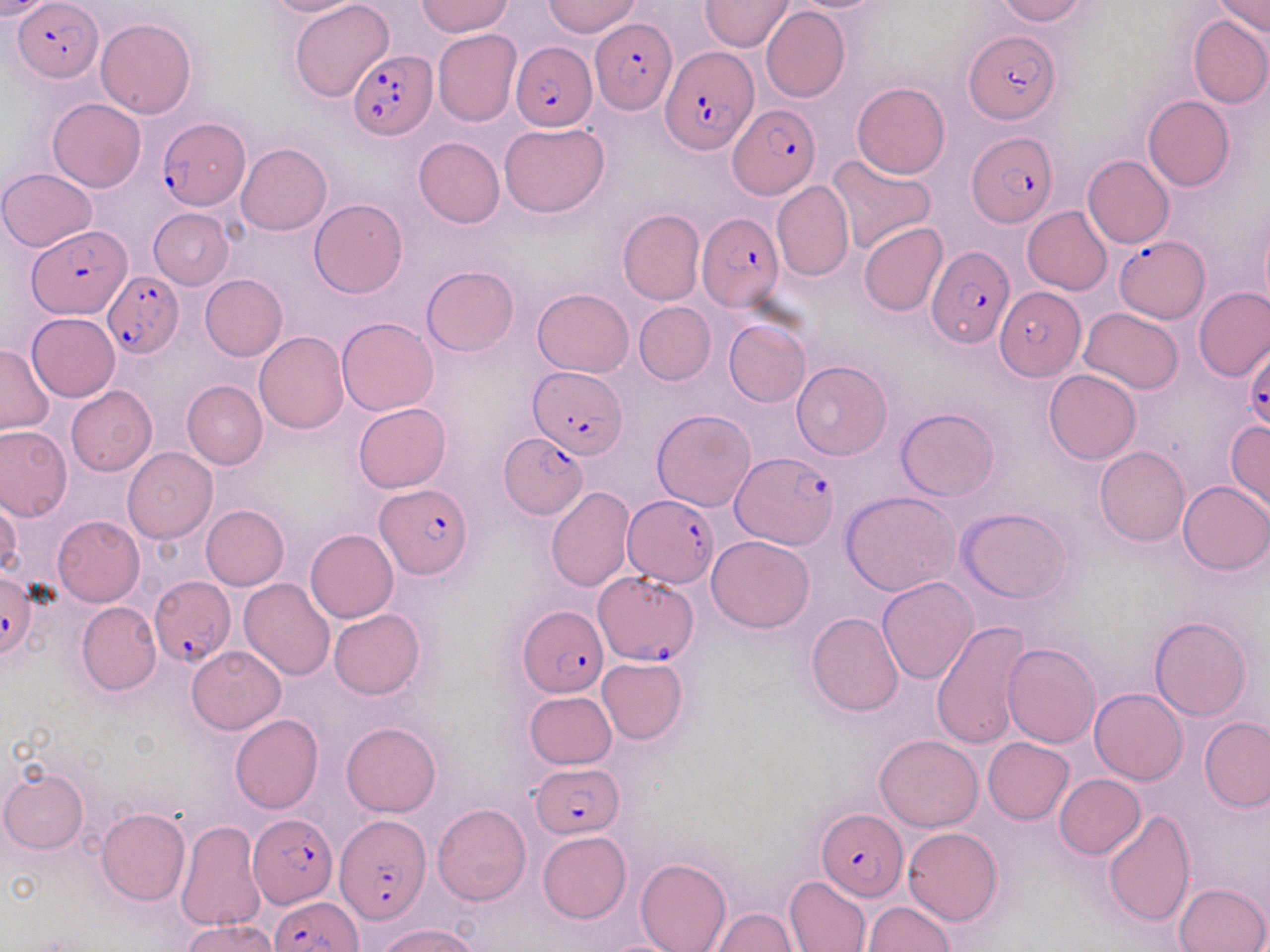
slide_level_diagnosis: Plasmodium falciparum
image_size: 1270×952 pixels
magnification: 1000x
modality: light microscopy
field_of_view: single
stain: May-Grünwald-Giemsa
uninfected_red_blood_cell_locations: 'approximate bounding boxes as (x1,y1)-(x2,y2) corner pairs in pixels: (0,0)-(56,19), (261,0)-(363,18), (543,0)-(640,37), (783,0)-(889,12), (995,0)-(1087,24), (1211,0)-(1269,38), (291,1)-(395,103), (417,1)-(513,37), (699,1)-(795,51), (761,5)-(850,102), (1188,14)-(1270,107), (96,18)-(197,118), (432,30)-(521,126), (851,82)-(949,179), (1143,95)-(1235,191), (47,98)-(146,192), (500,122)-(610,217), (413,136)-(505,228), (236,142)-(331,234), (826,153)-(936,253), (1084,155)-(1174,248), (0,169)-(98,251), (772,180)-(853,281), (309,199)-(407,298), (1023,205)-(1113,295), (149,208)-(234,289), (617,209)-(705,306), (1260,218)-(1270,317), (859,222)-(948,316), (422,266)-(519,357), (200,273)-(287,360), (1194,287)-(1270,382), (532,288)-(634,376), (634,302)-(715,385), (1080,308)-(1183,393), (27,313)-(121,400), (338,317)-(438,416), (723,319)-(809,407), (254,331)-(349,434), (0,344)-(53,434), (791,360)-(891,459), (1043,369)-(1140,464), (182,380)-(267,469), (66,386)-(156,475), (353,403)-(449,493), (896,407)-(998,501), (652,409)-(757,511), (1227,420)-(1270,513), (0,425)-(72,521), (1095,446)-(1189,545), (122,448)-(217,543), (1178,481)-(1270,574), (546,486)-(635,591), (842,491)-(959,596), (0,494)-(22,579), (200,504)-(289,590), (956,508)-(1070,602), (53,516)-(145,606), (306,528)-(398,623), (706,535)-(814,632), (878,576)-(979,684), (239,578)-(336,681), (76,601)-(161,696), (328,610)-(424,699), (806,612)-(903,716), (1149,616)-(1252,721), (931,619)-(1032,749), (1003,642)-(1100,746), (186,645)-(285,733), (597,656)-(688,744), (1090,687)-(1187,785), (524,691)-(616,768), (230,714)-(323,815), (1201,717)-(1270,814), (342,721)-(441,816), (875,734)-(984,831), (984,737)-(1073,824), (1,766)-(89,853), (1053,774)-(1145,859), (432,802)-(532,905), (96,808)-(190,904), (1102,808)-(1196,928), (175,819)-(266,932), (903,827)-(1002,925), (538,831)-(631,924), (635,857)-(731,952), (785,875)-(872,951), (1174,881)-(1269,952), (863,901)-(954,951), (712,908)-(798,950), (182,918)-(281,952), (377,923)-(483,952)'
plasmodium_falciparum_infected_red_blood_cell_locations: 'approximate bounding boxes as (x1,y1)-(x2,y2) corner pairs in pixels: (13,4)-(102,80), (586,18)-(675,114), (964,29)-(1058,124), (510,41)-(597,130), (662,45)-(758,154), (347,50)-(436,140), (727,104)-(820,199), (157,118)-(250,209), (967,131)-(1057,226), (697,214)-(782,312), (28,227)-(132,318), (1116,235)-(1208,322), (926,245)-(1013,349), (101,268)-(181,359), (994,287)-(1084,381), (1245,348)-(1270,431), (531,365)-(628,460), (500,434)-(589,519), (731,452)-(839,548), (375,483)-(473,577), (622,495)-(718,588), (1,570)-(39,657), (592,570)-(698,664), (148,577)-(234,670), (516,604)-(607,695), (532,761)-(625,838), (816,809)-(908,900), (245,815)-(334,911), (335,815)-(430,922), (267,897)-(362,952)'
preparation: thin blood film